Identify the parasite.
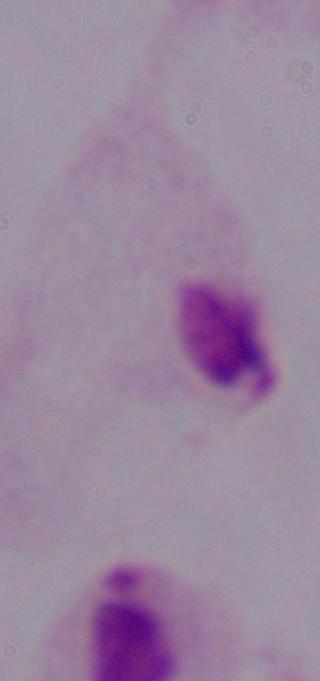
This is a trichomonad.

Captured at 1000x magnification. Photomicrograph.